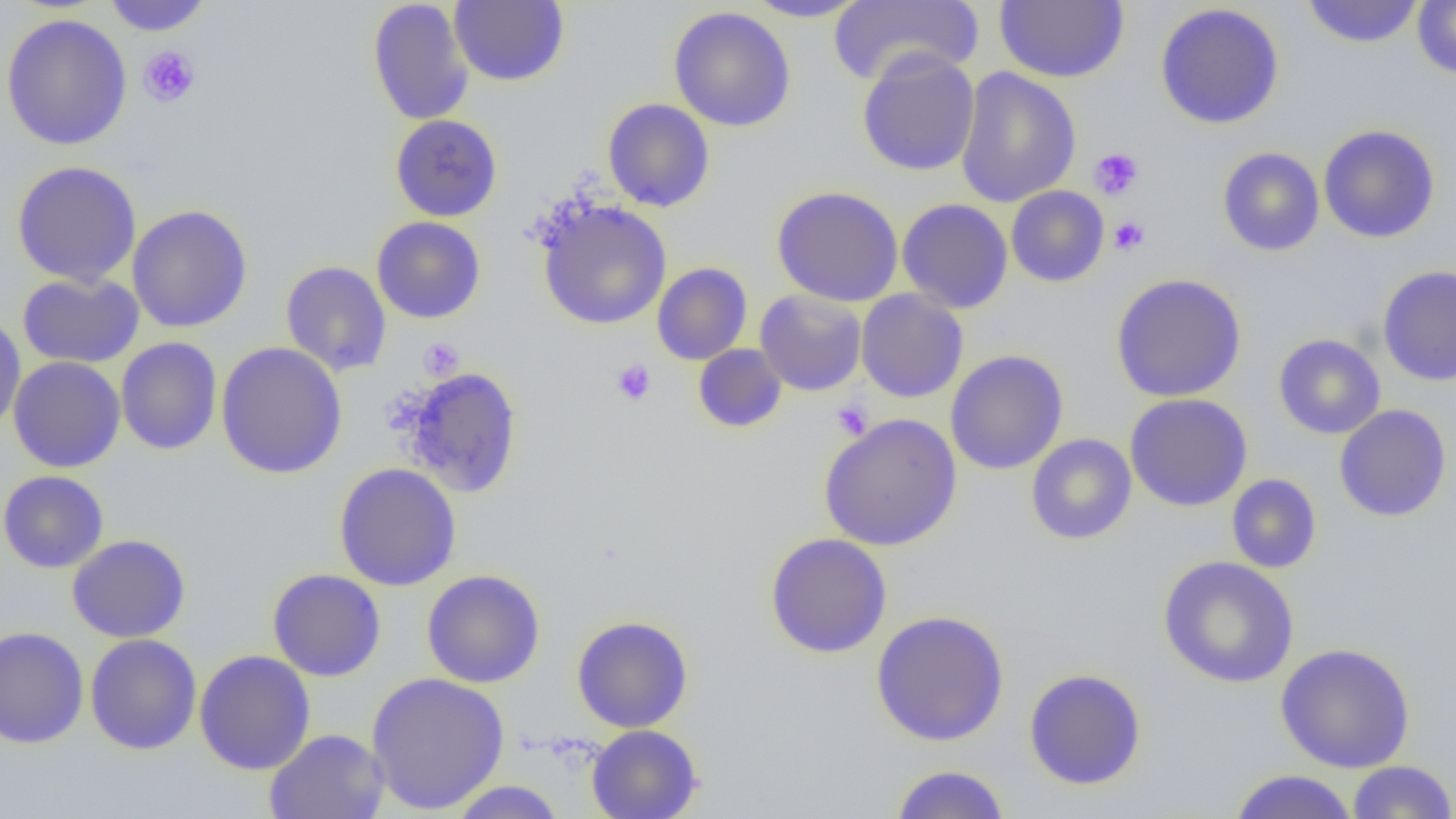

{
  "slide_level_diagnosis": "no evidence of blood parasites",
  "preparation": "thin blood film",
  "field_of_view": "single",
  "platelet_locations": "approximate bounding boxes as (x1, y1, x2, y2) in pixels: (138, 46, 201, 107), (1089, 147, 1144, 200), (1109, 217, 1149, 255), (418, 338, 464, 380), (611, 359, 656, 405), (831, 400, 872, 440)",
  "magnification": "1000x",
  "image_size": "1456×819 pixels",
  "modality": "light microscopy",
  "uninfected_red_blood_cell_locations": "approximate bounding boxes as (x1, y1, x2, y2) in pixels: (102, 0, 213, 36), (367, 0, 474, 126), (449, 0, 569, 87), (744, 0, 871, 22), (829, 0, 984, 87), (995, 0, 1128, 83), (1412, 0, 1456, 78), (1302, 1, 1424, 48), (1154, 3, 1285, 130), (668, 7, 796, 132), (1, 13, 132, 151), (856, 49, 980, 176), (955, 67, 1082, 209), (602, 98, 715, 212), (390, 114, 503, 222), (1318, 124, 1440, 243), (1216, 147, 1325, 256), (11, 160, 142, 286), (1006, 185, 1109, 287), (772, 186, 903, 306), (897, 198, 1013, 313), (538, 200, 672, 330), (127, 205, 253, 333), (371, 216, 486, 323), (280, 261, 392, 376), (652, 262, 752, 365), (1377, 265, 1456, 386), (17, 272, 144, 369), (1111, 273, 1246, 402), (754, 289, 867, 396), (856, 289, 968, 403), (0, 313, 26, 435), (1273, 333, 1386, 439), (115, 337, 222, 455), (216, 342, 347, 480), (693, 344, 788, 433), (945, 350, 1069, 475), (8, 356, 125, 473), (401, 367, 523, 497), (1124, 393, 1253, 512), (1334, 404, 1452, 522), (819, 413, 962, 551), (1025, 434, 1137, 545), (334, 463, 462, 591), (0, 470, 109, 573), (1226, 474, 1322, 574), (764, 532, 893, 658), (67, 534, 191, 643), (1158, 556, 1299, 688), (267, 568, 386, 681), (421, 569, 545, 688), (871, 610, 1010, 746), (572, 615, 694, 733), (0, 625, 89, 749), (85, 633, 202, 754), (1275, 643, 1416, 772), (194, 650, 316, 775), (1023, 668, 1147, 790), (366, 671, 509, 815), (587, 725, 703, 819), (265, 728, 390, 818), (1346, 761, 1456, 818), (888, 764, 1012, 818), (1228, 769, 1359, 819), (446, 780, 569, 818)"
}